Give the position of every Plasmodium falciparum parasite, noting its life-cycle stage.
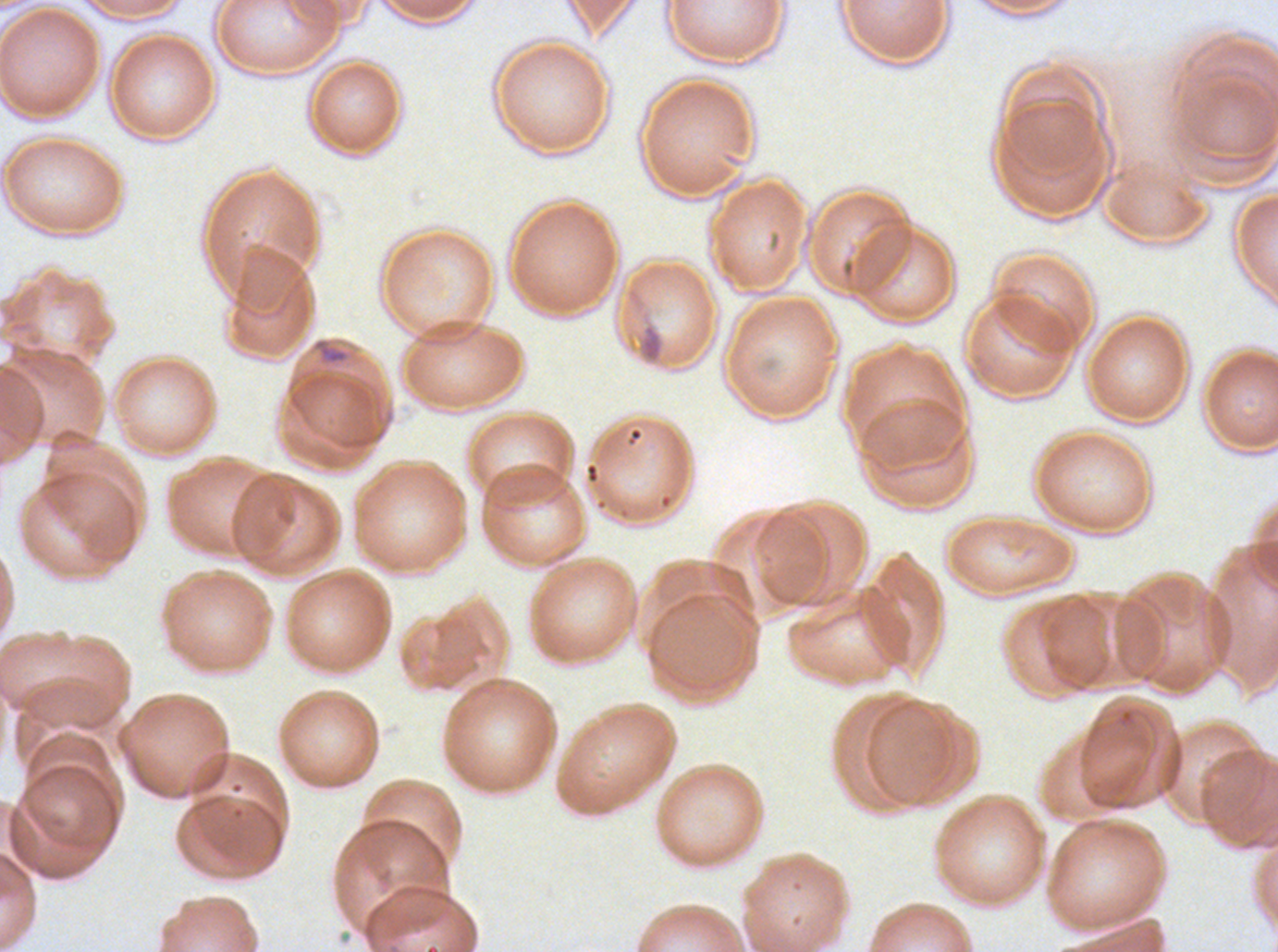
No rings, late-ring/early-trophozoite forms, mid trophozoites, late trophozoites, early schizonts, late schizonts, segmenters, or gametocytes observed.

Approximate bounding boxes as (x1, y1, x2, y2) in pixels. Debris locations: (636, 322, 665, 365), (312, 337, 350, 366). Thin blood smear. One sub-image of a larger composite. Plasmodium falciparum cultured ex vivo for 24 to 48 hours, from a patient in The Gambia. Giemsa-stained preparation. Image is 1278×952 pixels.